Classify this cell by malaria status.
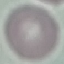
It is uninfected.

stain = Giemsa
image type = automatically extracted cell patch, resized to 64 × 64 pixels
capture = smartphone camera at the microscope eyepiece
preparation = thin blood film